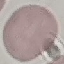
Result: negative for malaria parasites. Thin smear of blood. Giemsa-stained preparation. Cell patch, automatically extracted from a larger field of view and resized to 64 × 64 pixels. Acquired by smartphone through the microscope eyepiece.